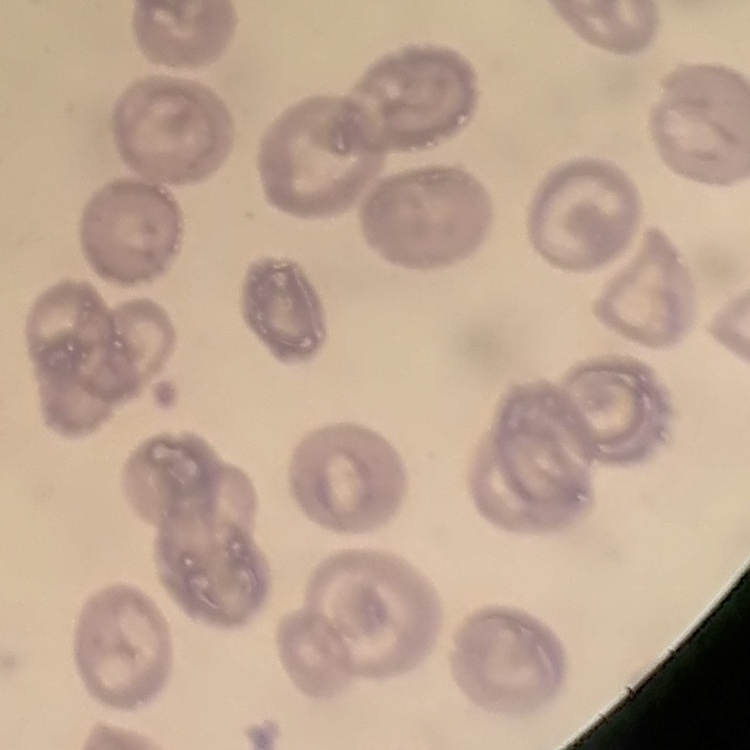

{
  "red_blood_cell_morphology": "no rouleaux formation",
  "preparation": "thin peripheral smear",
  "image_type": "one tile cut from a larger photomicrograph",
  "stain": "Field's or Giemsa"
}